State the blood parasite species.
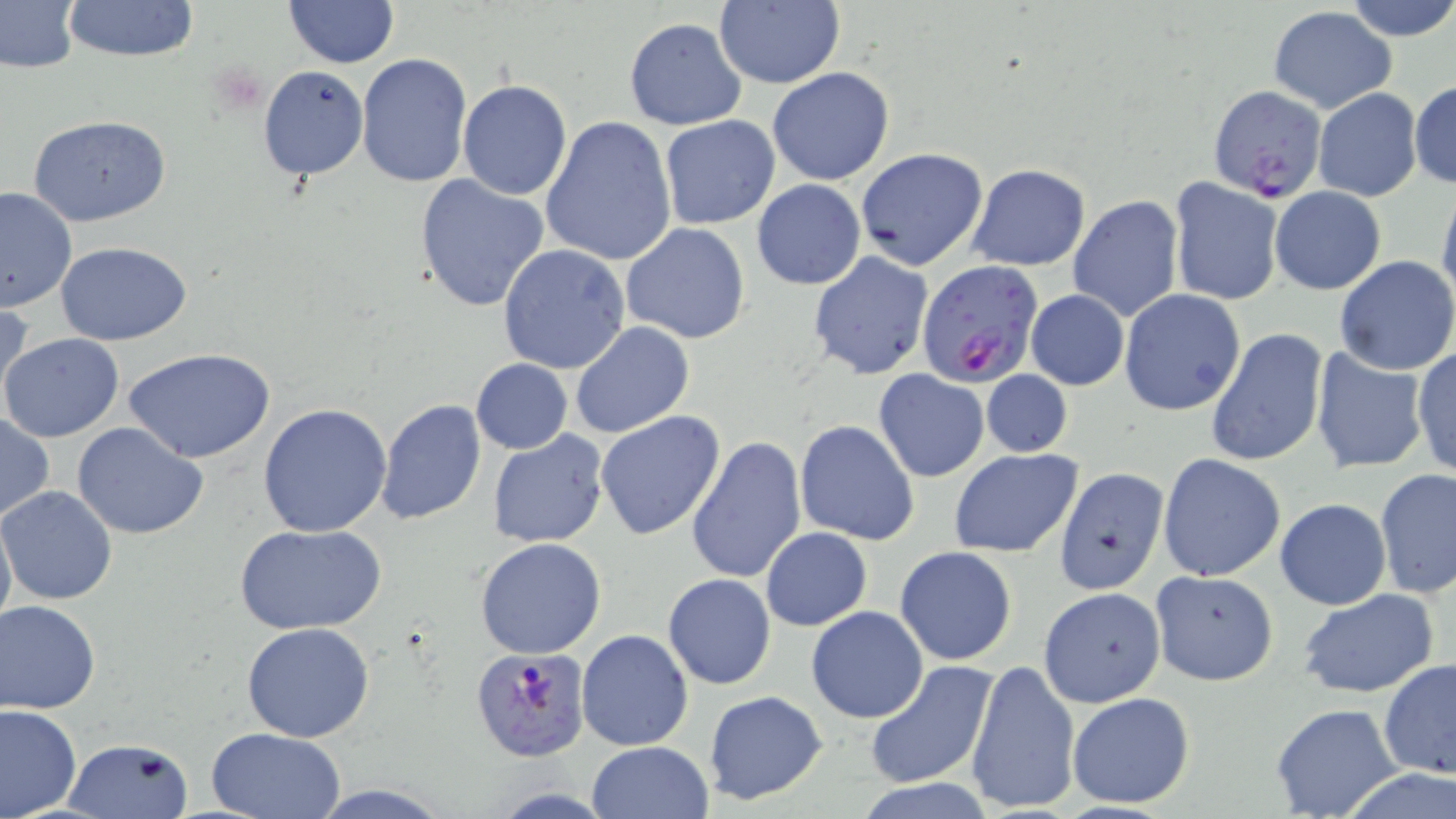
Plasmodium falciparum.

field_of_view: one of a larger specimen
image_size: 1456×819 pixels
modality: optical microscopy
stain: May-Grünwald-Giemsa
uninfected_red_blood_cell_locations: 'approximate bounding boxes as (x1,y1)-(x2,y2) corner pairs in pixels: (57,0)-(201,64), (1344,0)-(1456,42), (0,1)-(79,73), (283,1)-(399,68), (712,2)-(845,88), (1268,6)-(1397,113), (623,17)-(747,130), (355,53)-(474,189), (257,65)-(369,181), (768,66)-(895,185), (457,80)-(571,200), (1410,80)-(1455,189), (1313,88)-(1422,201), (28,114)-(171,227), (539,117)-(678,267), (660,117)-(781,229), (855,147)-(988,270), (966,162)-(1091,271), (414,171)-(550,312), (1169,176)-(1284,306), (751,178)-(866,290), (0,185)-(77,313), (1271,186)-(1386,294), (1436,187)-(1456,307), (1069,195)-(1183,322), (621,223)-(751,346), (57,243)-(191,346), (499,243)-(632,375), (808,251)-(933,381), (1334,257)-(1456,374), (1026,289)-(1129,390), (1120,290)-(1246,416), (0,299)-(33,420), (569,322)-(694,439), (1205,327)-(1328,466), (1,331)-(125,442), (1411,344)-(1456,481), (1309,346)-(1431,474), (121,347)-(276,464), (471,359)-(572,453), (873,368)-(990,483), (980,369)-(1072,458), (376,399)-(487,522), (258,403)-(393,539), (596,410)-(727,542), (0,413)-(54,523), (793,419)-(920,546), (72,421)-(208,538), (487,430)-(610,548), (688,435)-(806,585), (949,449)-(1082,559), (1158,453)-(1286,581), (1054,466)-(1169,594), (1375,468)-(1455,597), (1,486)-(119,605), (1275,499)-(1391,609), (0,506)-(15,639), (237,524)-(382,636), (761,527)-(872,629), (475,537)-(607,660), (895,547)-(1018,664), (1149,570)-(1278,685), (663,573)-(776,689), (1037,587)-(1165,708), (1297,589)-(1441,700), (1,600)-(101,714), (806,606)-(929,723), (242,621)-(375,743), (576,630)-(694,751), (966,658)-(1081,815), (1378,658)-(1456,779), (864,661)-(998,788), (703,691)-(830,806), (1066,691)-(1197,810), (1268,702)-(1407,818), (0,703)-(81,817), (206,728)-(345,818), (63,737)-(194,818), (587,741)-(714,819), (1336,767)-(1456,819), (853,779)-(998,817), (306,784)-(451,818)'
preparation: thin blood smear
plasmodium_falciparum_infected_red_blood_cell_locations: 'approximate bounding boxes as (x1,y1)-(x2,y2) corner pairs in pixels: (1208,86)-(1328,204), (916,260)-(1044,390), (470,646)-(591,760)'
magnification: 1000x